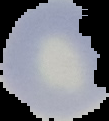
Summary:
  - Image size: 109×121 pixels
  - Result: no malaria parasites detected
  - Preparation: thin blood smear
  - Image type: segmented cell region on a black background